Locate every Plasmodium falciparum-infected red blood cell.
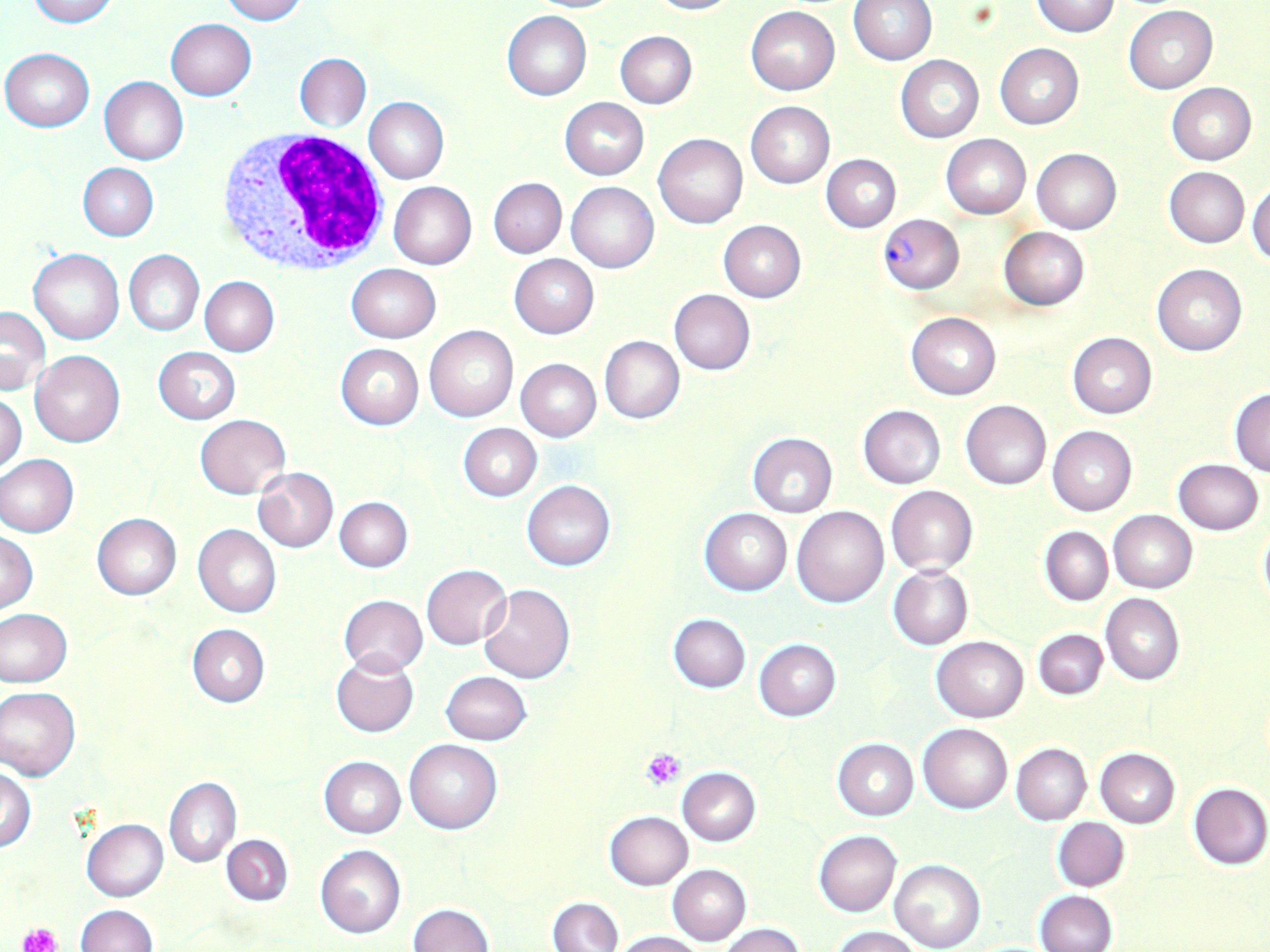
Approximate bounding boxes as named x1/y1/x2/y2 corners in pixels.
Plasmodium falciparum-infected red blood cells: (x1=879, y1=213, x2=964, y2=293).

Uninfected red blood cell locations: (x1=26, y1=0, x2=117, y2=27), (x1=217, y1=0, x2=307, y2=24), (x1=527, y1=0, x2=623, y2=13), (x1=645, y1=0, x2=739, y2=16), (x1=849, y1=1, x2=936, y2=65), (x1=1031, y1=1, x2=1120, y2=37), (x1=1125, y1=6, x2=1217, y2=93), (x1=745, y1=7, x2=839, y2=94), (x1=501, y1=10, x2=592, y2=100), (x1=166, y1=18, x2=255, y2=101), (x1=614, y1=30, x2=697, y2=109), (x1=994, y1=43, x2=1084, y2=129), (x1=1, y1=48, x2=95, y2=132), (x1=295, y1=53, x2=371, y2=131), (x1=896, y1=55, x2=984, y2=143), (x1=100, y1=76, x2=189, y2=165), (x1=1166, y1=82, x2=1257, y2=164), (x1=363, y1=96, x2=449, y2=184), (x1=560, y1=97, x2=648, y2=180), (x1=746, y1=101, x2=834, y2=188), (x1=654, y1=134, x2=748, y2=228), (x1=941, y1=134, x2=1031, y2=218), (x1=1032, y1=148, x2=1121, y2=233), (x1=822, y1=154, x2=901, y2=232), (x1=77, y1=162, x2=159, y2=241), (x1=1164, y1=166, x2=1250, y2=247), (x1=487, y1=177, x2=567, y2=258), (x1=1247, y1=180, x2=1269, y2=267), (x1=389, y1=181, x2=476, y2=270), (x1=567, y1=182, x2=658, y2=272), (x1=718, y1=220, x2=806, y2=302), (x1=999, y1=227, x2=1089, y2=310), (x1=28, y1=248, x2=124, y2=345), (x1=124, y1=249, x2=204, y2=337), (x1=509, y1=253, x2=599, y2=340), (x1=119, y1=262, x2=280, y2=345), (x1=1152, y1=264, x2=1247, y2=356), (x1=346, y1=265, x2=441, y2=343), (x1=200, y1=276, x2=279, y2=356), (x1=668, y1=289, x2=756, y2=375), (x1=0, y1=306, x2=50, y2=396), (x1=907, y1=311, x2=1001, y2=400), (x1=425, y1=326, x2=518, y2=421), (x1=1068, y1=333, x2=1157, y2=419), (x1=599, y1=336, x2=684, y2=424), (x1=335, y1=343, x2=424, y2=430), (x1=152, y1=346, x2=240, y2=425), (x1=30, y1=350, x2=125, y2=448), (x1=515, y1=359, x2=601, y2=442), (x1=1229, y1=388, x2=1270, y2=476), (x1=1, y1=392, x2=27, y2=476), (x1=960, y1=401, x2=1051, y2=490), (x1=858, y1=405, x2=945, y2=488), (x1=195, y1=415, x2=290, y2=499), (x1=458, y1=424, x2=542, y2=501), (x1=1047, y1=426, x2=1137, y2=516), (x1=747, y1=433, x2=838, y2=515), (x1=1, y1=454, x2=79, y2=536), (x1=1172, y1=459, x2=1264, y2=534), (x1=252, y1=468, x2=339, y2=552), (x1=522, y1=480, x2=614, y2=571), (x1=885, y1=486, x2=978, y2=575), (x1=334, y1=496, x2=413, y2=572), (x1=792, y1=505, x2=889, y2=608), (x1=700, y1=507, x2=792, y2=596), (x1=1108, y1=511, x2=1197, y2=592), (x1=92, y1=514, x2=182, y2=600), (x1=1257, y1=522, x2=1270, y2=613), (x1=192, y1=524, x2=281, y2=617), (x1=1039, y1=527, x2=1113, y2=606), (x1=1, y1=531, x2=39, y2=613), (x1=421, y1=564, x2=511, y2=649), (x1=888, y1=565, x2=973, y2=651), (x1=479, y1=584, x2=575, y2=683), (x1=1101, y1=593, x2=1184, y2=686), (x1=338, y1=595, x2=428, y2=675), (x1=1, y1=609, x2=72, y2=686), (x1=668, y1=614, x2=750, y2=692), (x1=186, y1=624, x2=269, y2=707), (x1=1033, y1=629, x2=1108, y2=701), (x1=932, y1=636, x2=1029, y2=722), (x1=754, y1=638, x2=841, y2=721), (x1=330, y1=654, x2=419, y2=737), (x1=441, y1=671, x2=532, y2=745), (x1=0, y1=686, x2=81, y2=780), (x1=919, y1=723, x2=1012, y2=813), (x1=404, y1=739, x2=502, y2=833), (x1=832, y1=739, x2=918, y2=820), (x1=1011, y1=743, x2=1091, y2=824), (x1=1095, y1=748, x2=1180, y2=828), (x1=319, y1=756, x2=406, y2=837), (x1=677, y1=767, x2=760, y2=846), (x1=0, y1=769, x2=36, y2=853), (x1=164, y1=778, x2=240, y2=867), (x1=1188, y1=783, x2=1270, y2=869), (x1=604, y1=811, x2=693, y2=890), (x1=1052, y1=817, x2=1130, y2=891), (x1=80, y1=818, x2=168, y2=901), (x1=814, y1=830, x2=901, y2=916), (x1=222, y1=834, x2=293, y2=906), (x1=315, y1=846, x2=406, y2=939), (x1=890, y1=859, x2=985, y2=952), (x1=667, y1=864, x2=751, y2=947), (x1=1034, y1=890, x2=1116, y2=952), (x1=547, y1=897, x2=622, y2=951), (x1=408, y1=902, x2=493, y2=952), (x1=75, y1=904, x2=158, y2=952), (x1=718, y1=924, x2=805, y2=952), (x1=832, y1=927, x2=921, y2=952), (x1=611, y1=930, x2=709, y2=952). Platelet locations: (x1=641, y1=747, x2=687, y2=791), (x1=19, y1=921, x2=61, y2=952). White blood cell locations: (x1=212, y1=128, x2=392, y2=275). Slide-level diagnosis: Plasmodium falciparum. Thin blood film. Light microscopy. May-Grünwald-Giemsa-stained preparation. One field of a larger specimen. Image is 1270×952 pixels. Captured at 1000x magnification.